State the preparation type.
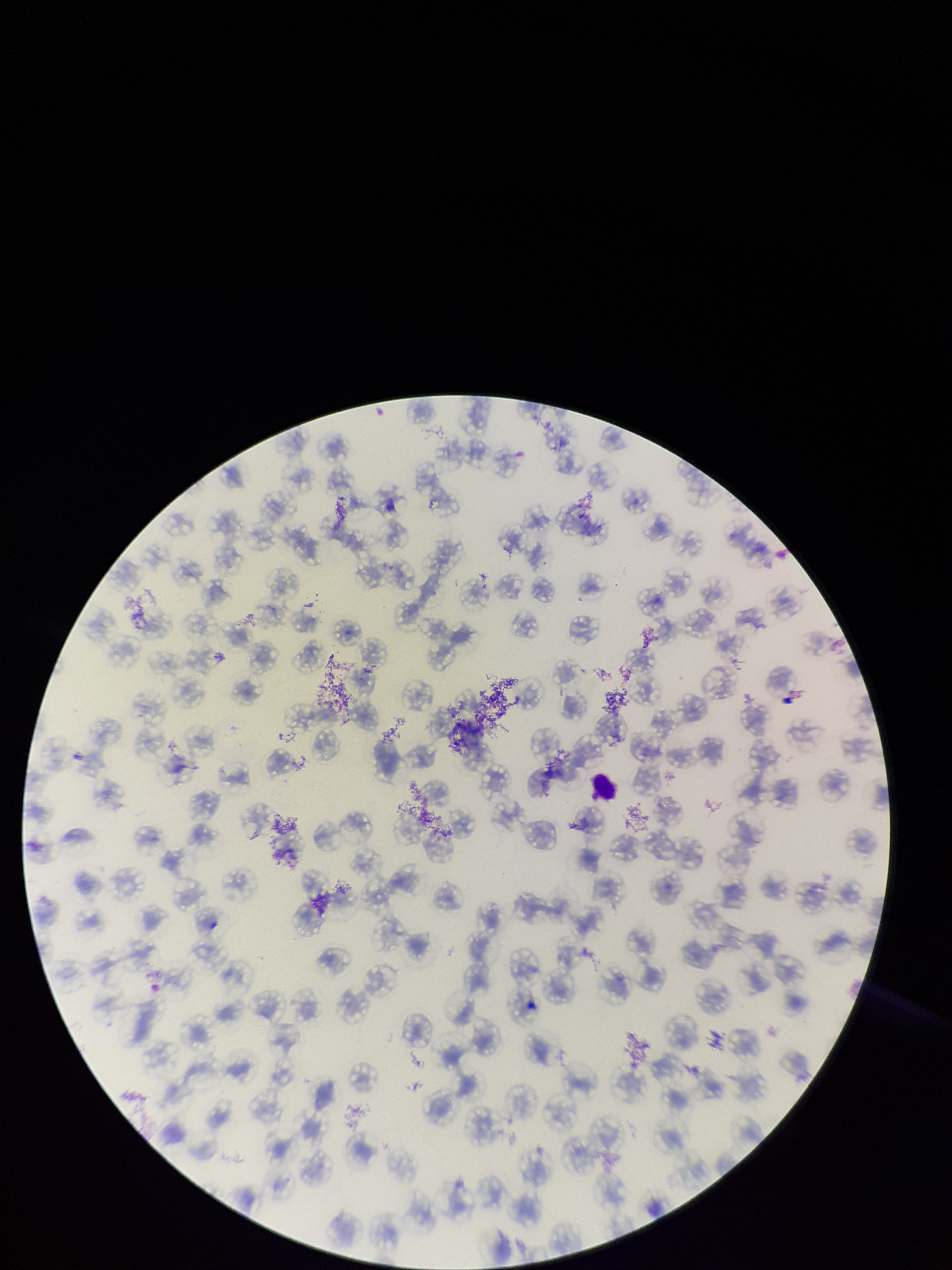
It is a thin blood smear.

Summary:
  - Parasitized red blood cell count: 0
  - Capture: smartphone photograph through the microscope eyepiece
  - Patient malaria status: positive
  - Parasitized red blood cells: none seen
  - Field of view: single
  - Species reported for this patient: Plasmodium falciparum
  - Red blood cell count: 127
  - Image size: 952×1270 pixels
  - Stain: Giemsa